Locate malaria parasites and leukocytes.
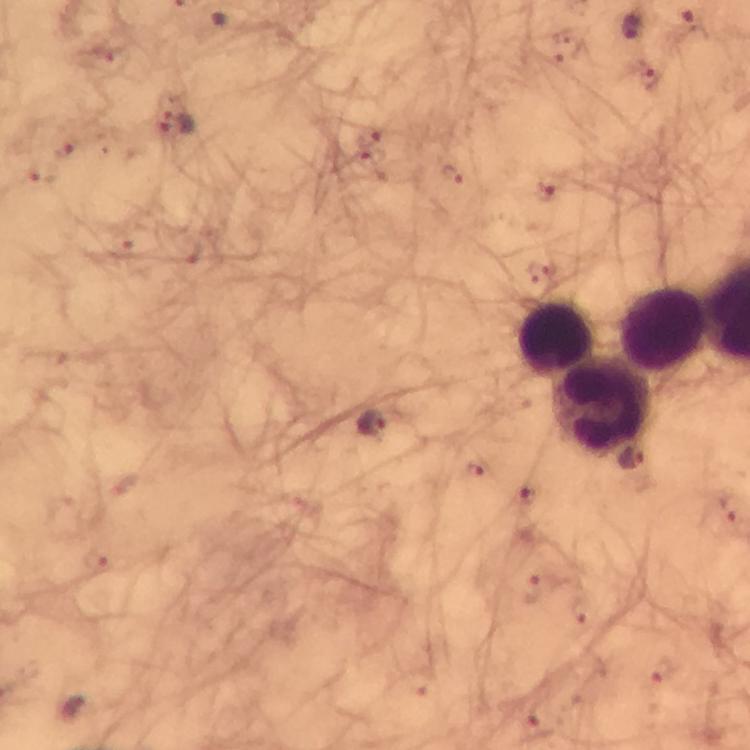

Approximate object centers, in pixels from the top-left corner.
Malaria parasites: (x=693, y=22), (x=630, y=25), (x=651, y=77), (x=177, y=122), (x=451, y=178), (x=373, y=422).
Leukocytes: (x=662, y=330), (x=556, y=340), (x=603, y=405).

Cropped region of a single field of view. Thick smear. From a diagnostic examination for malaria. Image is 750×750 pixels. Immersion oil applied. At 100x magnification. Smartphone photograph taken through a microscope. Giemsa-stained preparation.